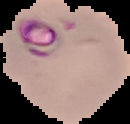

preparation = thin blood film
malaria status = parasitized
image type = segmented cell region with the area outside set to black
image size = 130×124 pixels